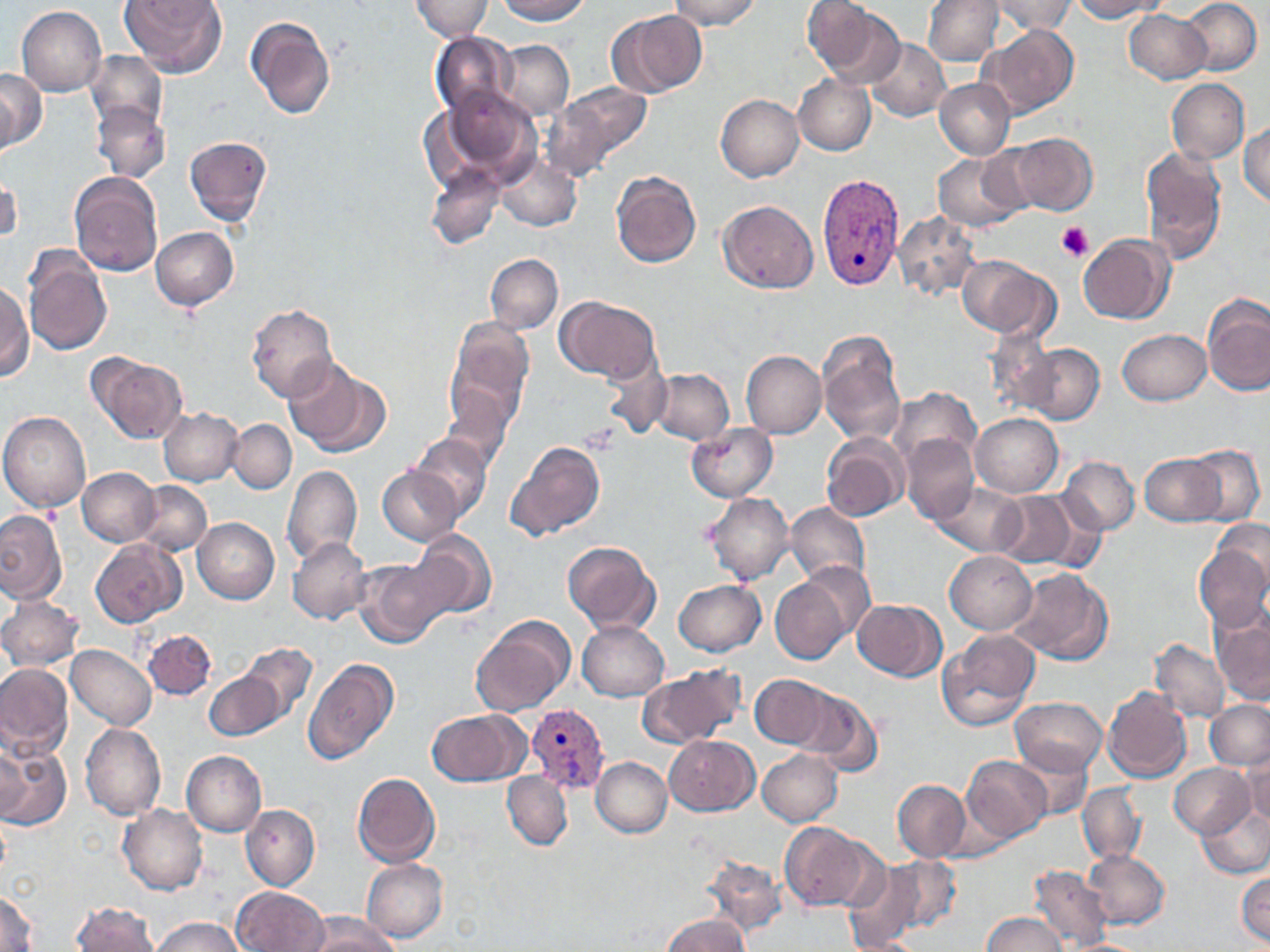

Summary:
  - Coordinate format: approximate bounding boxes as [x1, y1, x2, y2] in pixels
  - Plasmodium vivax-infected red blood cell locations: [817, 173, 905, 291], [527, 704, 608, 792]
  - Platelet locations: [1056, 223, 1094, 263], [580, 424, 622, 454]
  - Uninfected red blood cell locations: [120, 0, 226, 78], [409, 0, 493, 41], [496, 0, 592, 24], [668, 0, 760, 30], [924, 0, 1002, 66], [993, 0, 1077, 35], [1071, 0, 1165, 21], [1181, 0, 1261, 75], [803, 1, 896, 83], [16, 6, 106, 96], [608, 9, 707, 99], [1124, 10, 1211, 84], [246, 16, 336, 119], [980, 25, 1077, 120], [430, 32, 517, 119], [866, 38, 949, 121], [494, 40, 574, 120], [85, 52, 168, 132], [0, 66, 45, 152], [793, 76, 875, 154], [934, 78, 1015, 159], [1167, 79, 1250, 164], [548, 82, 650, 174], [436, 86, 543, 184], [715, 95, 804, 182], [91, 101, 170, 184], [1240, 122, 1269, 206], [1009, 133, 1098, 215], [184, 135, 272, 226], [1140, 147, 1227, 262], [495, 154, 581, 231], [933, 154, 1022, 230], [424, 162, 505, 250], [611, 170, 701, 268], [1, 171, 21, 247], [68, 172, 163, 278], [718, 199, 819, 293], [892, 212, 980, 299], [151, 226, 239, 310], [1078, 234, 1175, 324], [23, 250, 112, 354], [485, 254, 562, 333], [958, 256, 1055, 339], [0, 284, 32, 381], [1202, 296, 1270, 397], [556, 297, 660, 383], [245, 305, 338, 403], [445, 317, 534, 432], [1118, 329, 1210, 404], [985, 331, 1059, 417], [817, 332, 905, 447], [1018, 341, 1104, 424], [740, 350, 826, 438], [89, 353, 186, 444], [284, 359, 390, 458], [601, 361, 672, 438], [650, 369, 734, 444], [889, 387, 980, 470], [442, 392, 514, 471], [158, 408, 243, 485], [0, 412, 92, 511], [971, 413, 1063, 497], [227, 418, 297, 493], [686, 424, 778, 502], [901, 433, 980, 525], [407, 434, 494, 522], [821, 435, 909, 524], [506, 441, 606, 541], [1185, 445, 1265, 525], [1140, 452, 1225, 526], [1060, 456, 1139, 534], [282, 465, 362, 565], [377, 466, 460, 545], [77, 467, 160, 546], [134, 481, 212, 557], [933, 483, 1027, 555], [990, 490, 1079, 569], [703, 492, 794, 585], [786, 502, 870, 587], [0, 510, 65, 603], [192, 518, 278, 603], [1212, 519, 1270, 595], [408, 530, 497, 619], [288, 536, 372, 625], [90, 539, 185, 627], [562, 541, 659, 634], [1193, 545, 1270, 631], [945, 550, 1036, 634], [353, 557, 451, 647], [791, 560, 877, 646], [1007, 567, 1113, 666], [772, 573, 852, 663], [673, 577, 765, 657], [0, 595, 85, 671], [852, 598, 946, 680], [1210, 604, 1270, 705], [471, 617, 574, 715], [577, 621, 669, 702], [143, 629, 217, 700], [937, 629, 1040, 730], [1150, 639, 1229, 722], [238, 642, 317, 723], [66, 645, 156, 730], [303, 658, 399, 764], [0, 663, 73, 758], [639, 666, 745, 749], [204, 670, 284, 741], [751, 674, 832, 749], [1102, 686, 1192, 783], [791, 688, 881, 775], [1009, 696, 1108, 776], [1204, 700, 1270, 770], [427, 709, 528, 787], [80, 722, 165, 821], [665, 734, 759, 817], [0, 744, 70, 830], [1, 744, 29, 823], [1014, 748, 1092, 820], [757, 749, 842, 826], [181, 751, 266, 836], [1240, 751, 1270, 828], [962, 755, 1051, 843], [590, 757, 672, 837], [1169, 763, 1252, 837], [502, 771, 572, 850], [352, 772, 440, 867], [893, 780, 971, 861], [1077, 783, 1147, 866], [1196, 802, 1270, 877], [119, 804, 207, 895], [241, 805, 320, 890], [780, 823, 873, 911], [1084, 848, 1170, 928], [700, 855, 787, 937], [884, 856, 961, 933], [362, 859, 448, 942], [842, 860, 923, 951], [1027, 865, 1113, 951], [1236, 871, 1270, 947], [232, 887, 328, 951], [0, 891, 40, 952], [72, 903, 161, 952], [662, 912, 749, 952], [981, 912, 1070, 952], [306, 913, 398, 952], [151, 917, 245, 952], [1058, 938, 1154, 951]
  - Slide-level diagnosis: Plasmodium vivax
  - Stain: May-Grünwald-Giemsa
  - Field of view: one of a larger specimen
  - Image size: 1270×952 pixels
  - Preparation: thin blood smear
  - Modality: light microscopy
  - Magnification: 1000x